Assess the morphology of the erythrocytes.
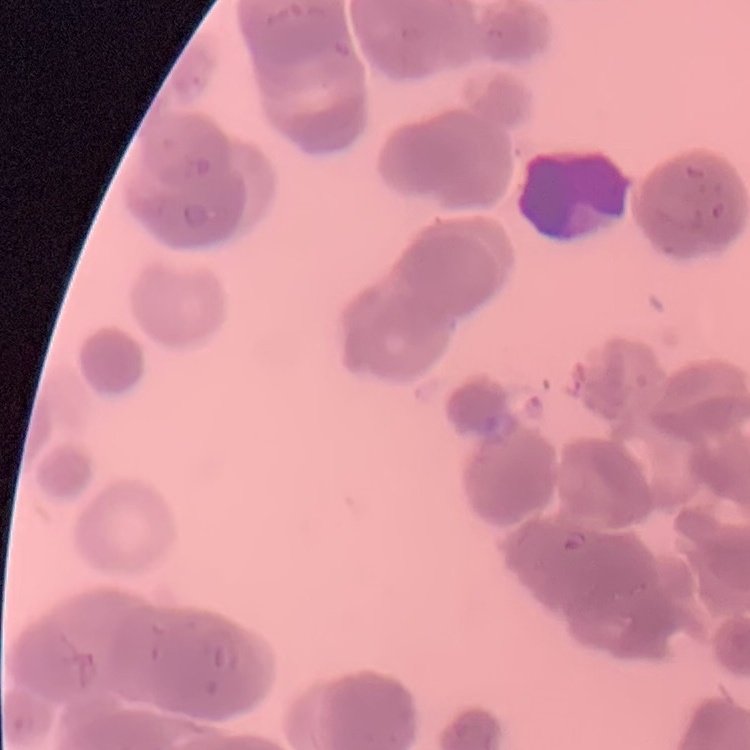

Rouleaux formation.

Summary:
  - Image type: one tile cut from a larger photomicrograph
  - Preparation: thin blood film
  - Stain: Field's or Giemsa